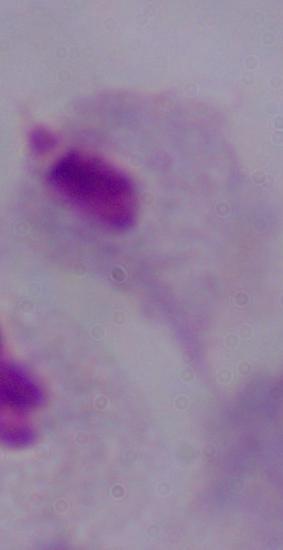
A trichomonad is seen. 1000x magnification. Photomicrograph.